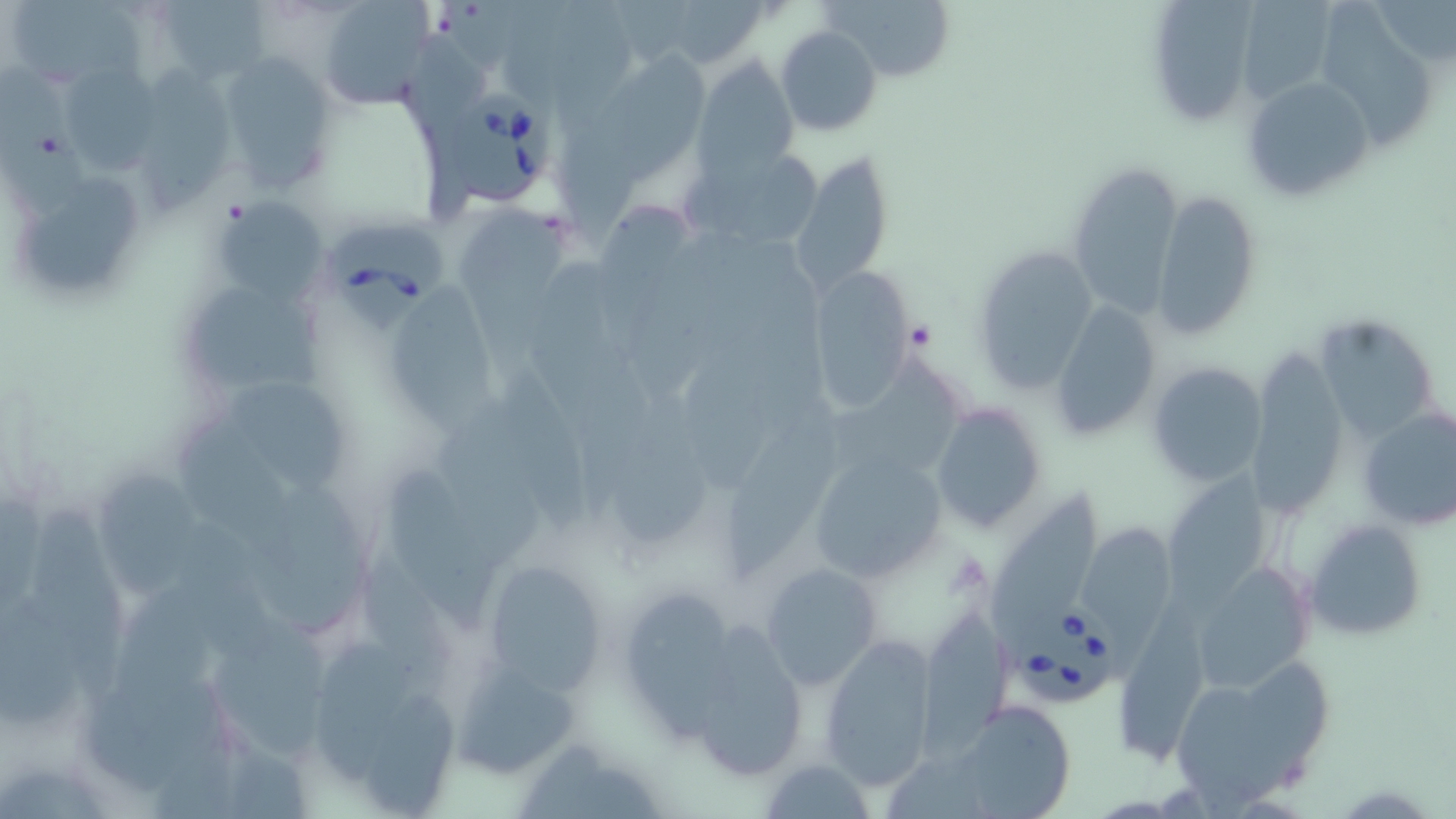
slide-level diagnosis = Babesia divergens
image size = 1456×819 pixels
platelet locations = approximate bounding boxes as named x1/y1/x2/y2 corners in pixels: (x1=906, y1=320, x2=936, y2=351)
preparation = thin blood smear
uninfected red blood cell locations = approximate bounding boxes as named x1/y1/x2/y2 corners in pixels: (x1=15, y1=0, x2=153, y2=84), (x1=155, y1=0, x2=270, y2=87), (x1=316, y1=0, x2=433, y2=108), (x1=656, y1=0, x2=768, y2=69), (x1=1140, y1=0, x2=1263, y2=125), (x1=1248, y1=0, x2=1332, y2=97), (x1=1314, y1=0, x2=1435, y2=151), (x1=824, y1=1, x2=959, y2=83), (x1=774, y1=25, x2=883, y2=138), (x1=405, y1=30, x2=495, y2=218), (x1=610, y1=47, x2=719, y2=185), (x1=216, y1=52, x2=339, y2=198), (x1=136, y1=57, x2=232, y2=213), (x1=694, y1=57, x2=798, y2=180), (x1=58, y1=61, x2=166, y2=176), (x1=0, y1=62, x2=91, y2=216), (x1=1237, y1=74, x2=1375, y2=203), (x1=558, y1=100, x2=644, y2=255), (x1=687, y1=145, x2=825, y2=249), (x1=793, y1=150, x2=894, y2=293), (x1=1068, y1=165, x2=1181, y2=317), (x1=29, y1=178, x2=144, y2=292), (x1=1152, y1=190, x2=1261, y2=339), (x1=209, y1=197, x2=330, y2=305), (x1=598, y1=201, x2=691, y2=287), (x1=459, y1=203, x2=571, y2=396), (x1=531, y1=257, x2=616, y2=419), (x1=807, y1=268, x2=915, y2=411), (x1=390, y1=279, x2=501, y2=452), (x1=181, y1=288, x2=325, y2=388), (x1=1052, y1=299, x2=1165, y2=442), (x1=1315, y1=314, x2=1439, y2=445), (x1=823, y1=355, x2=968, y2=474), (x1=1146, y1=359, x2=1270, y2=486), (x1=1248, y1=359, x2=1347, y2=521), (x1=494, y1=369, x2=588, y2=533), (x1=233, y1=379, x2=349, y2=496), (x1=619, y1=393, x2=710, y2=545), (x1=726, y1=399, x2=847, y2=580), (x1=931, y1=402, x2=1047, y2=533), (x1=1356, y1=405, x2=1456, y2=530), (x1=181, y1=422, x2=302, y2=570), (x1=435, y1=425, x2=537, y2=562), (x1=804, y1=449, x2=951, y2=589), (x1=388, y1=462, x2=493, y2=631), (x1=96, y1=464, x2=202, y2=593), (x1=1164, y1=468, x2=1266, y2=624), (x1=257, y1=484, x2=367, y2=639), (x1=989, y1=489, x2=1100, y2=644), (x1=35, y1=507, x2=130, y2=704), (x1=1307, y1=520, x2=1428, y2=640), (x1=1077, y1=521, x2=1175, y2=684), (x1=178, y1=522, x2=273, y2=665), (x1=376, y1=557, x2=458, y2=704), (x1=480, y1=557, x2=613, y2=697), (x1=760, y1=560, x2=883, y2=690), (x1=1192, y1=561, x2=1317, y2=693), (x1=0, y1=590, x2=87, y2=729), (x1=626, y1=590, x2=736, y2=741), (x1=1120, y1=596, x2=1213, y2=765), (x1=918, y1=611, x2=1010, y2=767), (x1=704, y1=618, x2=807, y2=776), (x1=211, y1=621, x2=327, y2=761), (x1=314, y1=635, x2=413, y2=780), (x1=822, y1=638, x2=938, y2=789), (x1=1165, y1=663, x2=1327, y2=805), (x1=461, y1=668, x2=579, y2=768), (x1=365, y1=688, x2=472, y2=814), (x1=952, y1=701, x2=1075, y2=817), (x1=155, y1=728, x2=242, y2=819), (x1=762, y1=756, x2=875, y2=819), (x1=0, y1=766, x2=112, y2=819)
modality = optical microscopy
field of view = one of a larger specimen
Babesia divergens-infected red blood cell locations = approximate bounding boxes as named x1/y1/x2/y2 corners in pixels: (x1=447, y1=92, x2=562, y2=216), (x1=327, y1=222, x2=450, y2=333), (x1=1014, y1=607, x2=1122, y2=709)
stain = May-Grünwald-Giemsa
magnification = 1000x